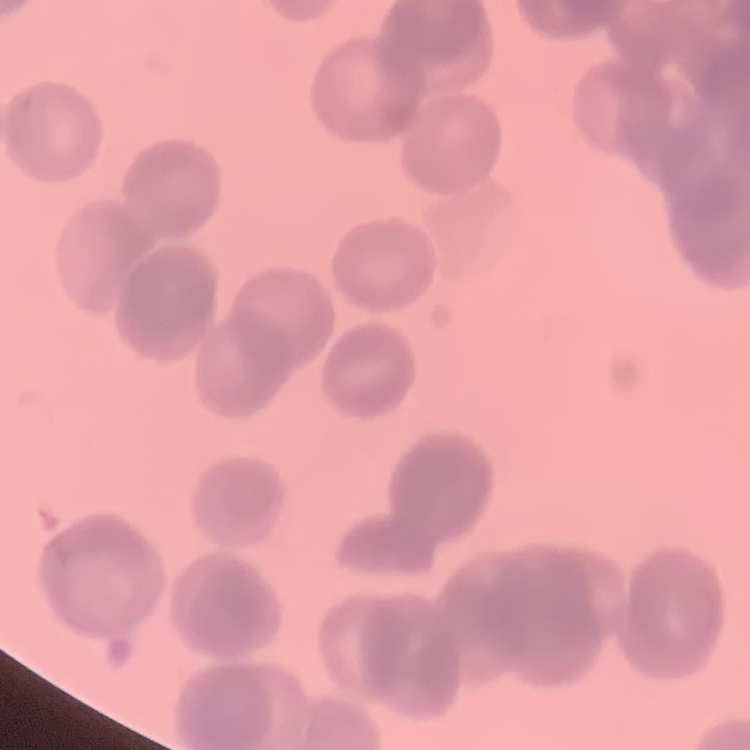

{
  "erythrocyte_morphology": "rouleaux formation",
  "image_type": "square crop of a larger photomicrograph",
  "stain": "Field's or Giemsa",
  "preparation": "thin blood smear"
}